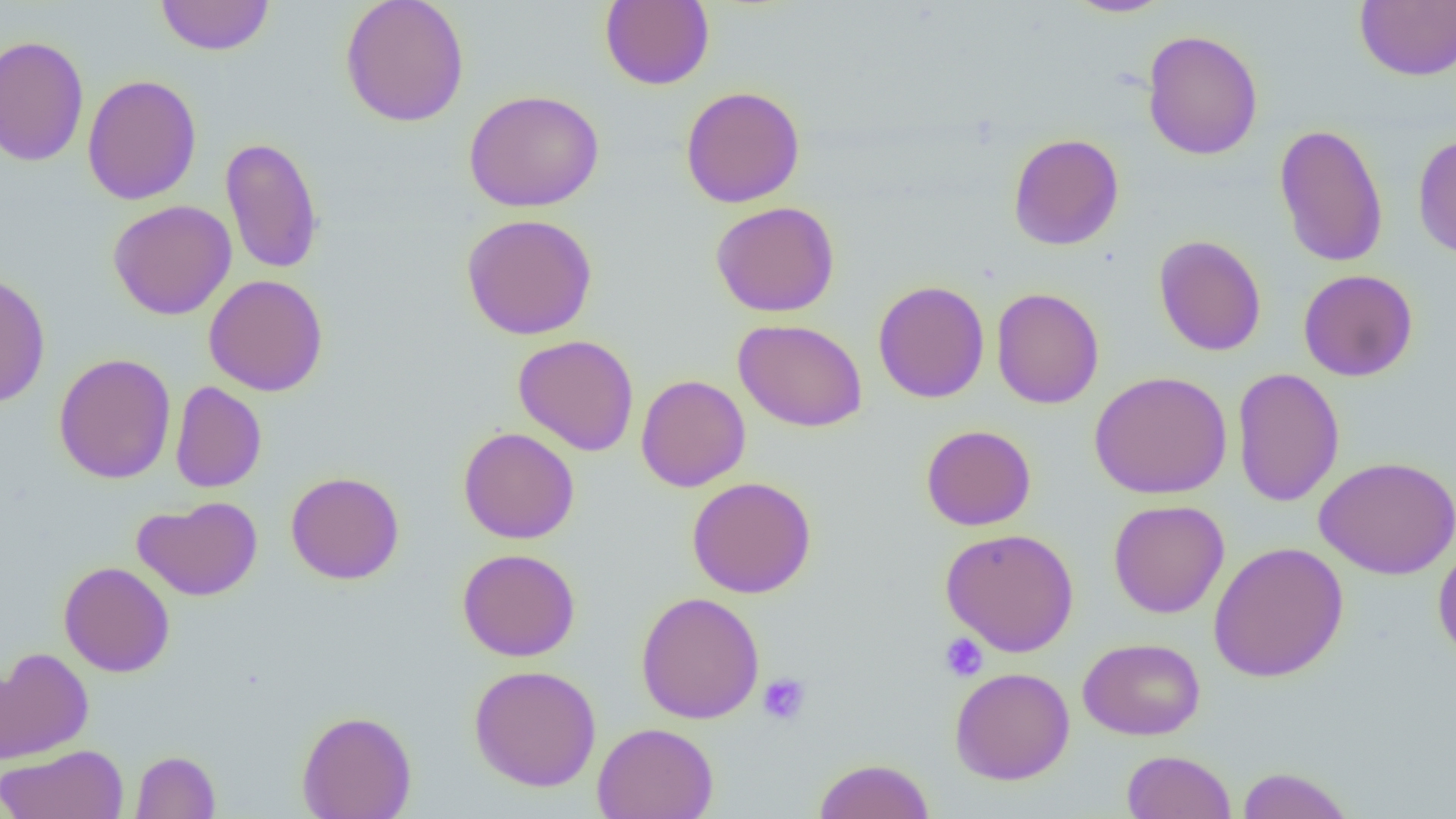
Approximate bounding boxes as named x1/y1/x2/y2 corners in pixels. Platelet locations: (x1=940, y1=632, x2=988, y2=681), (x1=757, y1=673, x2=811, y2=726). Uninfected red blood cell locations: (x1=156, y1=0, x2=274, y2=56), (x1=340, y1=0, x2=470, y2=127), (x1=599, y1=0, x2=715, y2=90), (x1=1064, y1=0, x2=1173, y2=18), (x1=1355, y1=0, x2=1456, y2=81), (x1=1142, y1=29, x2=1264, y2=161), (x1=0, y1=35, x2=90, y2=167), (x1=82, y1=74, x2=202, y2=205), (x1=680, y1=86, x2=805, y2=208), (x1=464, y1=89, x2=604, y2=212), (x1=1273, y1=123, x2=1388, y2=268), (x1=1412, y1=132, x2=1456, y2=261), (x1=1008, y1=133, x2=1124, y2=251), (x1=220, y1=136, x2=324, y2=275), (x1=108, y1=200, x2=236, y2=320), (x1=711, y1=201, x2=840, y2=317), (x1=461, y1=213, x2=598, y2=340), (x1=1153, y1=234, x2=1267, y2=356), (x1=1298, y1=269, x2=1419, y2=382), (x1=0, y1=270, x2=51, y2=409), (x1=204, y1=275, x2=328, y2=396), (x1=873, y1=280, x2=990, y2=403), (x1=991, y1=287, x2=1104, y2=409), (x1=733, y1=319, x2=867, y2=432), (x1=513, y1=334, x2=640, y2=456), (x1=53, y1=353, x2=177, y2=484), (x1=1231, y1=367, x2=1345, y2=507), (x1=1089, y1=370, x2=1232, y2=499), (x1=635, y1=374, x2=750, y2=492), (x1=170, y1=381, x2=267, y2=492), (x1=920, y1=424, x2=1036, y2=531), (x1=458, y1=427, x2=580, y2=544), (x1=1315, y1=455, x2=1456, y2=580), (x1=285, y1=471, x2=405, y2=585), (x1=686, y1=476, x2=816, y2=598), (x1=132, y1=496, x2=263, y2=602), (x1=1108, y1=500, x2=1229, y2=618), (x1=940, y1=528, x2=1079, y2=657), (x1=1208, y1=541, x2=1349, y2=683), (x1=1432, y1=543, x2=1456, y2=663), (x1=457, y1=548, x2=581, y2=662), (x1=59, y1=561, x2=175, y2=677), (x1=635, y1=591, x2=765, y2=724), (x1=1078, y1=637, x2=1205, y2=740), (x1=0, y1=647, x2=94, y2=765), (x1=469, y1=664, x2=602, y2=792), (x1=950, y1=666, x2=1075, y2=785), (x1=296, y1=709, x2=417, y2=819), (x1=592, y1=722, x2=719, y2=819), (x1=0, y1=744, x2=128, y2=819), (x1=130, y1=750, x2=220, y2=818), (x1=1123, y1=750, x2=1236, y2=819), (x1=813, y1=758, x2=935, y2=818), (x1=1235, y1=766, x2=1355, y2=819). Slide-level diagnosis: no evidence of blood parasites. Image is 1456×819 pixels. One field of a larger specimen. Optical microscopy. Captured at 1000x magnification. Thin blood film.